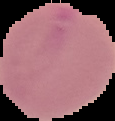
Summary:
  - Malaria status: uninfected
  - Preparation: thin blood film
  - Image type: cell region segmented out of the field of view; surrounding area masked to black
  - Image size: 115×121 pixels